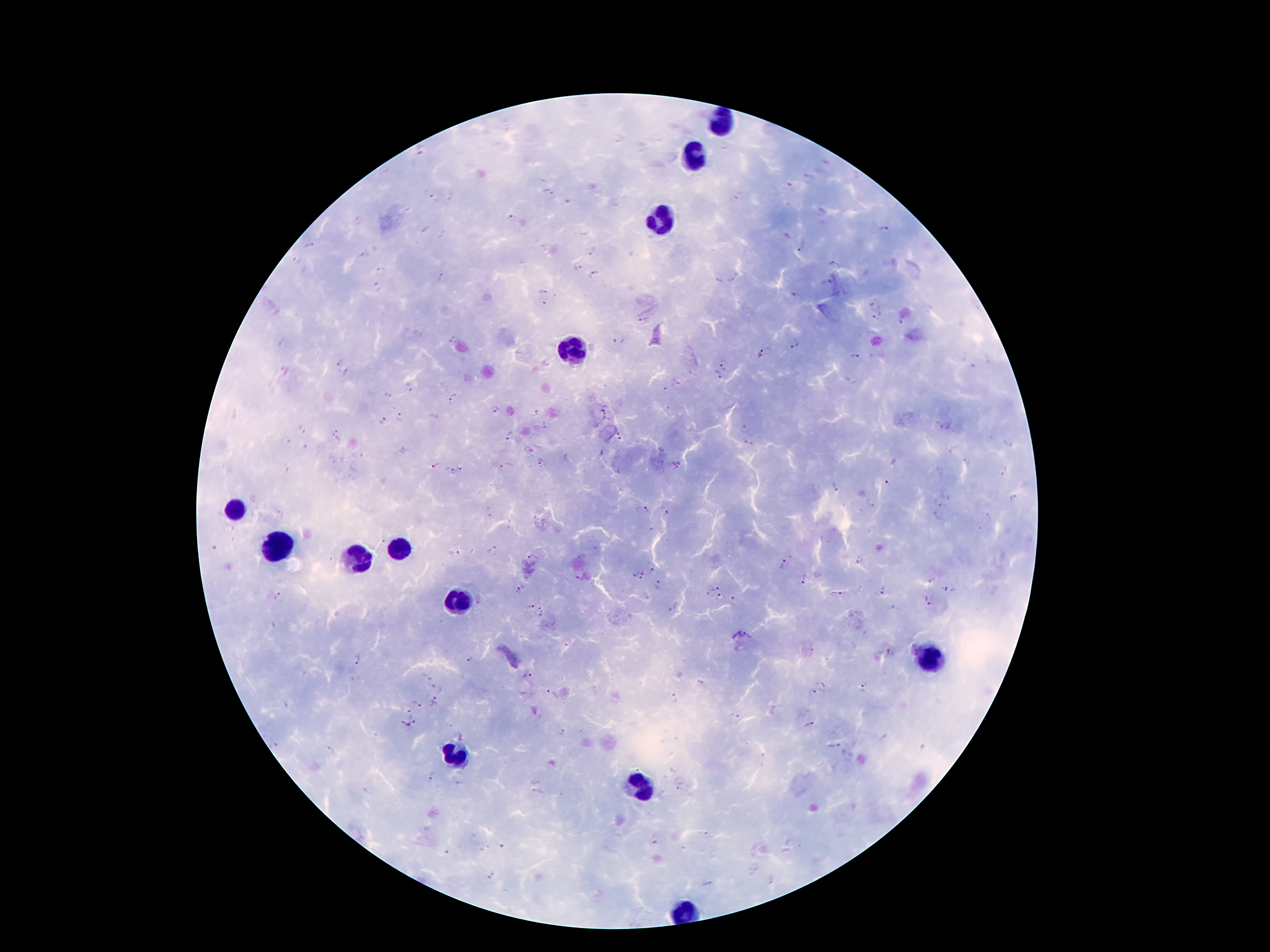

Approximate centers as {x, y} in pixels.
Summary:
  - Leukocyte locations: {723, 121}, {693, 156}, {666, 215}, {575, 348}, {234, 511}, {276, 543}, {397, 548}, {357, 556}, {456, 598}, {931, 664}, {454, 758}, {634, 788}, {683, 916}
  - Malaria parasite locations: {420, 150}, {809, 180}, {554, 195}, {738, 196}, {433, 198}, {452, 198}, {512, 219}, {358, 222}, {885, 231}, {309, 246}, {801, 250}, {592, 253}, {365, 256}, {834, 265}, {381, 268}, {577, 268}, {595, 274}, {438, 277}, {733, 280}, {377, 289}, {543, 290}, {794, 296}, {872, 307}, {877, 317}, {643, 320}, {902, 320}, {619, 341}, {452, 342}, {792, 345}, {761, 355}, {855, 357}, {339, 362}, {725, 363}, {717, 378}, {410, 387}, {388, 394}, {454, 397}, {607, 408}, {495, 409}, {536, 412}, {401, 417}, {382, 419}, {743, 427}, {302, 430}, {334, 432}, {510, 435}, {620, 437}, {286, 440}, {748, 444}, {541, 462}, {966, 462}, {434, 465}, {676, 467}, {501, 468}, {462, 469}, {450, 471}, {1004, 474}, {886, 483}, {833, 486}, {1015, 500}, {869, 505}, {943, 506}, {641, 509}, {664, 513}, {935, 517}, {491, 549}, {456, 554}, {532, 557}, {857, 561}, {652, 567}, {785, 567}, {639, 575}, {932, 580}, {802, 581}, {658, 585}, {714, 585}, {884, 589}, {949, 589}, {518, 591}, {837, 593}, {709, 594}, {279, 596}, {721, 598}, {735, 600}, {928, 603}, {528, 607}, {895, 608}, {543, 613}, {748, 635}, {889, 652}, {356, 658}, {471, 659}, {530, 675}, {701, 682}, {824, 683}, {438, 686}, {864, 687}, {813, 693}, {553, 694}, {671, 698}, {416, 701}, {434, 701}, {408, 711}, {736, 718}, {810, 726}, {409, 727}, {562, 732}, {463, 735}, {834, 745}, {331, 750}, {432, 777}, {538, 794}, {655, 844}
  - Image size: 1270×952 pixels
  - Magnification: 100x
  - Stain: Giemsa
  - Field of view: one from this slide
  - Patient malaria status: positive for Plasmodium falciparum
  - Capture: smartphone camera through the microscope eyepiece
  - Preparation: thick peripheral-blood smear